Classify this cell by malaria status.
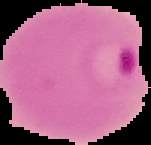
It is parasitized.

Image is 151×145 pixels. Cell region segmented out of the field of view; the surrounding area is masked to black. From a thin blood smear.